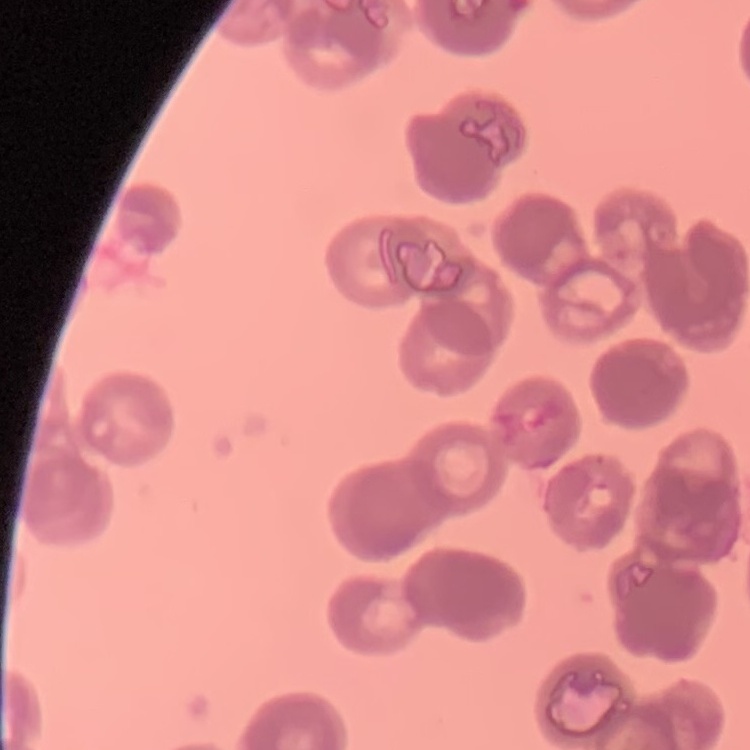
erythrocyte morphology = rouleaux formation
preparation = thin blood film
image type = square crop of a larger photomicrograph
stain = Field's or Giemsa